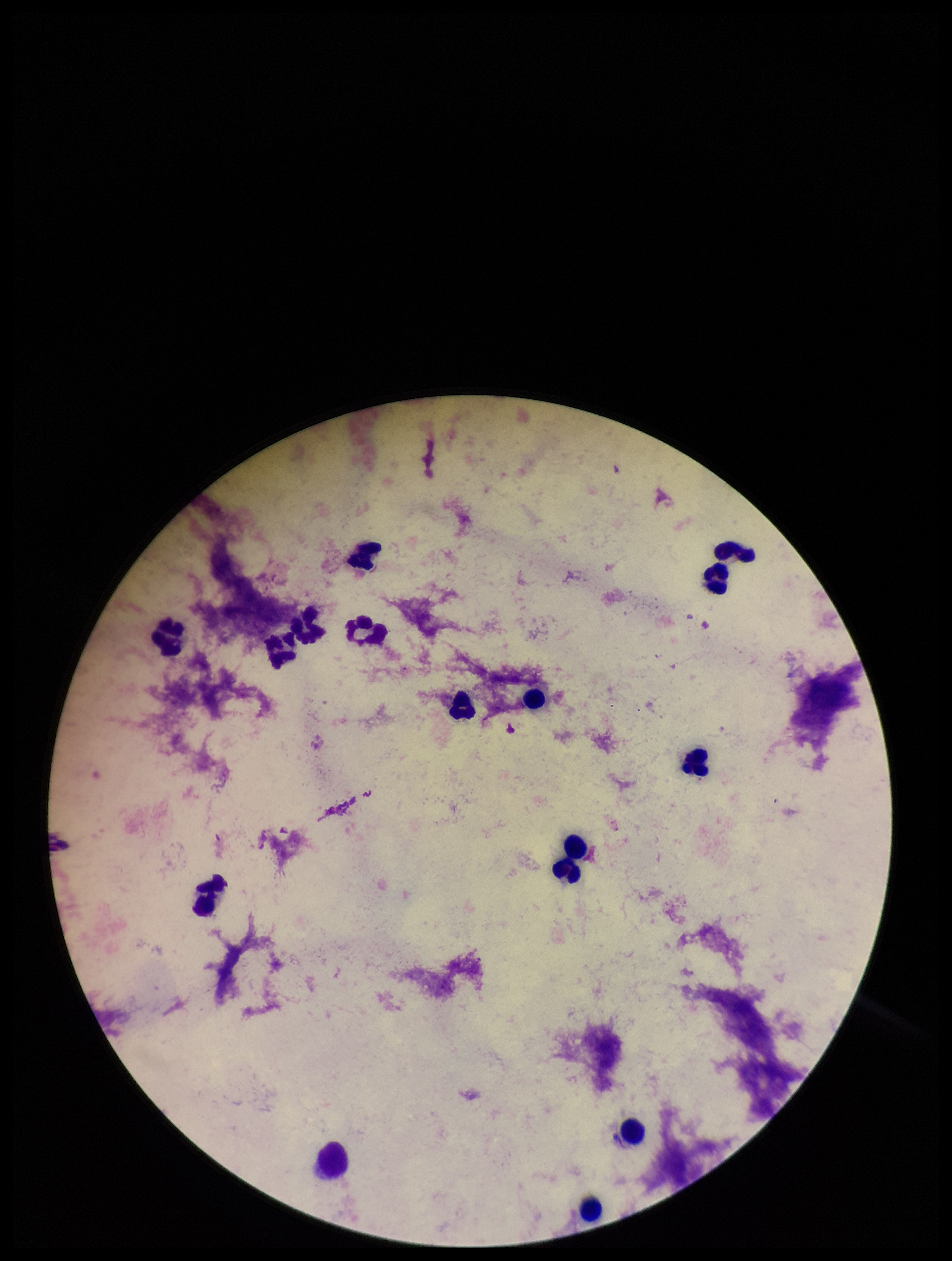
capture = smartphone photograph through the microscope eyepiece
preparation = thick
leukocyte count = 15
field of view = one from this slide
Plasmodium parasites = none detected
stain = Giemsa
image size = 952×1261 pixels
patient malaria status = negative
parasite count = 0